Look for Plasmodium parasites.
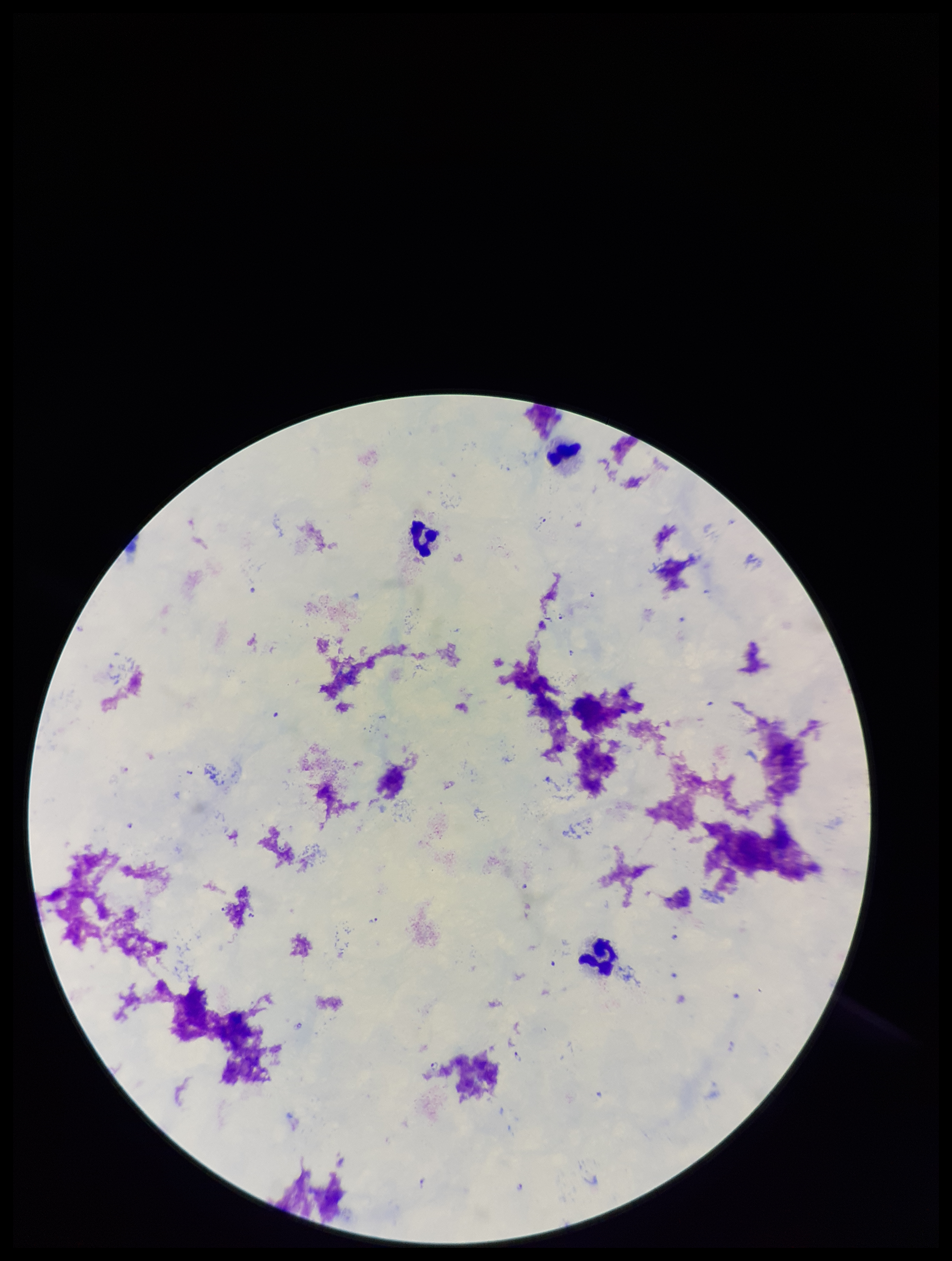

Detected.

Summary:
  - Field of view: one from this slide
  - Stain: Giemsa
  - Image size: 952×1261 pixels
  - Leukocyte count: 3
  - Preparation: thick smear
  - Capture: smartphone photograph through the microscope eyepiece
  - Patient malaria status: infected
  - Parasite count: 13
  - Species reported for this patient: Plasmodium falciparum